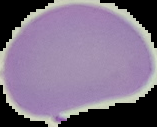

Image is 157×127 pixels. Result: no Plasmodium parasites seen. Segmented cell region on a black background. From a thin blood film.